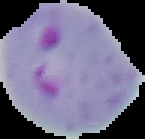

Summary:
  - Preparation: thin blood film
  - Image type: segmented cell region on a black background
  - Image size: 145×139 pixels
  - Result: malaria parasites identified